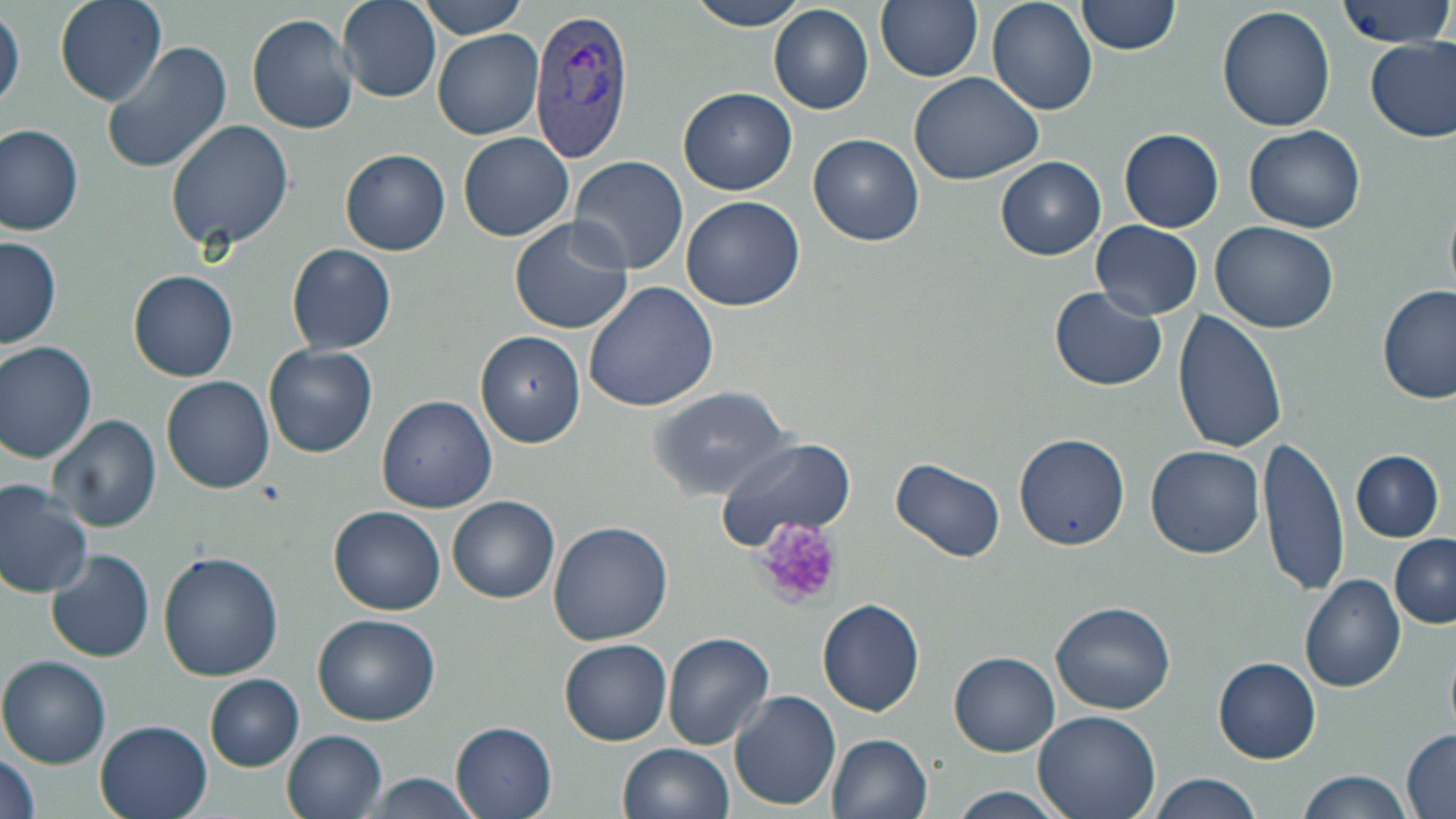
slide-level diagnosis = Plasmodium vivax
uninfected red blood cell locations = approximate bounding boxes as named x1/y1/x2/y2 corners in pixels: (x1=50, y1=0, x2=168, y2=105), (x1=338, y1=0, x2=441, y2=101), (x1=417, y1=0, x2=530, y2=39), (x1=686, y1=0, x2=810, y2=31), (x1=876, y1=0, x2=983, y2=82), (x1=989, y1=0, x2=1098, y2=114), (x1=1077, y1=0, x2=1183, y2=56), (x1=1332, y1=0, x2=1456, y2=50), (x1=770, y1=4, x2=874, y2=114), (x1=1217, y1=5, x2=1337, y2=132), (x1=0, y1=6, x2=23, y2=113), (x1=246, y1=12, x2=360, y2=135), (x1=433, y1=29, x2=543, y2=139), (x1=1366, y1=37, x2=1456, y2=143), (x1=101, y1=40, x2=232, y2=176), (x1=909, y1=71, x2=1044, y2=184), (x1=679, y1=88, x2=798, y2=195), (x1=164, y1=118, x2=295, y2=254), (x1=0, y1=123, x2=85, y2=234), (x1=1245, y1=124, x2=1366, y2=235), (x1=1119, y1=128, x2=1224, y2=232), (x1=458, y1=132, x2=575, y2=241), (x1=809, y1=133, x2=925, y2=247), (x1=341, y1=148, x2=451, y2=255), (x1=570, y1=154, x2=691, y2=274), (x1=997, y1=156, x2=1105, y2=259), (x1=681, y1=195, x2=803, y2=312), (x1=510, y1=217, x2=632, y2=334), (x1=1091, y1=220, x2=1204, y2=319), (x1=1210, y1=220, x2=1339, y2=333), (x1=2, y1=235, x2=63, y2=349), (x1=287, y1=244, x2=397, y2=355), (x1=129, y1=271, x2=239, y2=382), (x1=582, y1=280, x2=719, y2=413), (x1=1377, y1=283, x2=1454, y2=404), (x1=1049, y1=287, x2=1168, y2=390), (x1=1173, y1=309, x2=1287, y2=454), (x1=474, y1=330, x2=585, y2=446), (x1=1, y1=340, x2=98, y2=463), (x1=264, y1=344, x2=377, y2=457), (x1=161, y1=375, x2=275, y2=493), (x1=647, y1=385, x2=795, y2=499), (x1=377, y1=395, x2=498, y2=514), (x1=47, y1=414, x2=161, y2=534), (x1=1013, y1=434, x2=1129, y2=549), (x1=1260, y1=436, x2=1349, y2=595), (x1=716, y1=438, x2=855, y2=548), (x1=1146, y1=445, x2=1265, y2=559), (x1=1351, y1=450, x2=1445, y2=541), (x1=891, y1=457, x2=1005, y2=562), (x1=0, y1=480, x2=93, y2=597), (x1=447, y1=495, x2=560, y2=603), (x1=331, y1=505, x2=445, y2=614), (x1=549, y1=520, x2=672, y2=644), (x1=1390, y1=533, x2=1456, y2=628), (x1=47, y1=548, x2=153, y2=661), (x1=158, y1=551, x2=285, y2=681), (x1=1299, y1=574, x2=1406, y2=692), (x1=816, y1=599, x2=926, y2=717), (x1=1051, y1=601, x2=1177, y2=714), (x1=312, y1=613, x2=440, y2=725), (x1=662, y1=632, x2=774, y2=749), (x1=559, y1=637, x2=672, y2=745), (x1=951, y1=653, x2=1059, y2=755), (x1=0, y1=655, x2=113, y2=768), (x1=1214, y1=658, x2=1320, y2=761), (x1=206, y1=675, x2=303, y2=770), (x1=730, y1=690, x2=841, y2=810), (x1=1034, y1=710, x2=1159, y2=819), (x1=94, y1=718, x2=214, y2=819), (x1=452, y1=720, x2=558, y2=819), (x1=1401, y1=727, x2=1456, y2=819), (x1=283, y1=729, x2=386, y2=819), (x1=825, y1=733, x2=932, y2=819), (x1=621, y1=743, x2=734, y2=819), (x1=0, y1=745, x2=40, y2=819), (x1=1298, y1=771, x2=1413, y2=819), (x1=358, y1=772, x2=486, y2=817), (x1=1147, y1=773, x2=1263, y2=819), (x1=950, y1=786, x2=1065, y2=819)
Plasmodium vivax-infected red blood cell locations = approximate bounding boxes as named x1/y1/x2/y2 corners in pixels: (x1=527, y1=2, x2=638, y2=165)
modality = optical microscopy
preparation = thin blood film
image size = 1456×819 pixels
field of view = one of a larger specimen
magnification = 1000x
platelet locations = approximate bounding boxes as named x1/y1/x2/y2 corners in pixels: (x1=756, y1=520, x2=842, y2=609)
stain = May-Grünwald-Giemsa